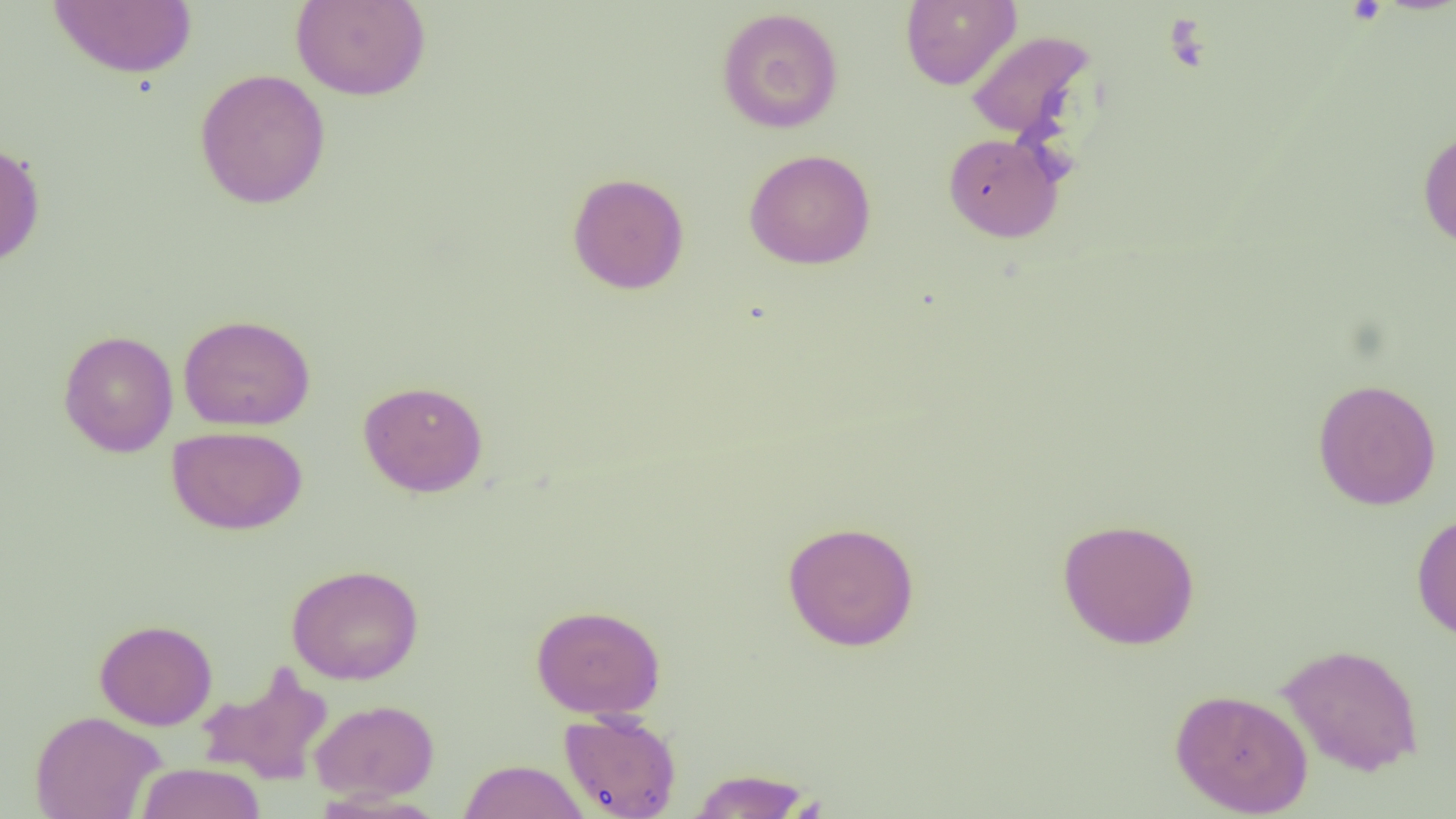
slide-level diagnosis = negative for blood parasites
magnification = 1000x
preparation = thin blood film
modality = optical microscopy
image size = 1456×819 pixels
uninfected red blood cell locations = approximate bounding boxes as named x1/y1/x2/y2 corners in pixels: (x1=47, y1=0, x2=199, y2=79), (x1=291, y1=0, x2=430, y2=101), (x1=900, y1=0, x2=1021, y2=90), (x1=716, y1=7, x2=844, y2=134), (x1=966, y1=30, x2=1095, y2=142), (x1=194, y1=68, x2=331, y2=209), (x1=1417, y1=127, x2=1456, y2=250), (x1=943, y1=132, x2=1064, y2=242), (x1=0, y1=141, x2=46, y2=268), (x1=744, y1=149, x2=876, y2=270), (x1=567, y1=172, x2=690, y2=295), (x1=178, y1=314, x2=315, y2=431), (x1=58, y1=330, x2=178, y2=457), (x1=1312, y1=378, x2=1442, y2=510), (x1=358, y1=380, x2=488, y2=497), (x1=167, y1=426, x2=307, y2=534), (x1=1411, y1=511, x2=1456, y2=642), (x1=1057, y1=517, x2=1200, y2=650), (x1=782, y1=520, x2=920, y2=652), (x1=286, y1=563, x2=424, y2=685), (x1=531, y1=604, x2=665, y2=719), (x1=94, y1=619, x2=218, y2=730), (x1=1278, y1=643, x2=1424, y2=776), (x1=197, y1=663, x2=334, y2=785), (x1=1170, y1=687, x2=1313, y2=817), (x1=310, y1=698, x2=439, y2=801), (x1=30, y1=710, x2=165, y2=819), (x1=558, y1=710, x2=682, y2=819), (x1=457, y1=759, x2=591, y2=819), (x1=135, y1=762, x2=266, y2=819), (x1=686, y1=768, x2=815, y2=818)
field of view = single